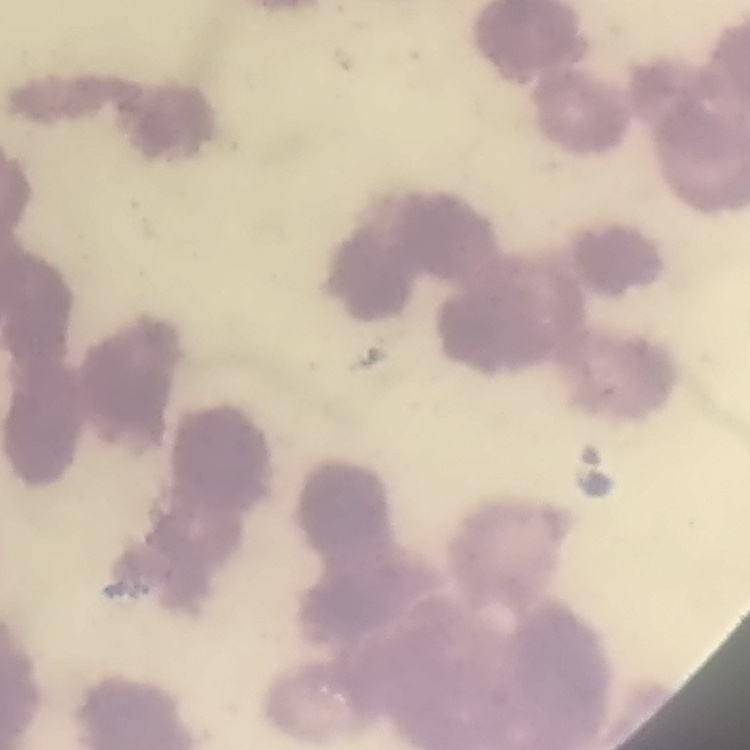
red_blood_cell_morphology: rouleaux formation
preparation: thin blood smear
stain: Field's or Giemsa
image_type: square crop of a larger photomicrograph